State which cell type is depicted.
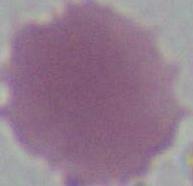
This is an erythrocyte.

Summary:
  - Magnification: 1000x
  - Modality: micrograph